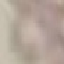

Malaria status: uninfected. Thin blood smear. Giemsa stain. Acquired by smartphone through the microscope eyepiece. Automatically extracted cell patch, resized to 64 × 64 pixels.